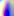
identification = Toxoplasma gondii
magnification = 400x
modality = micrograph